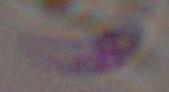 Toxoplasma gondii is shown. Captured at 1000x magnification. Micrograph.